State the blood parasite species.
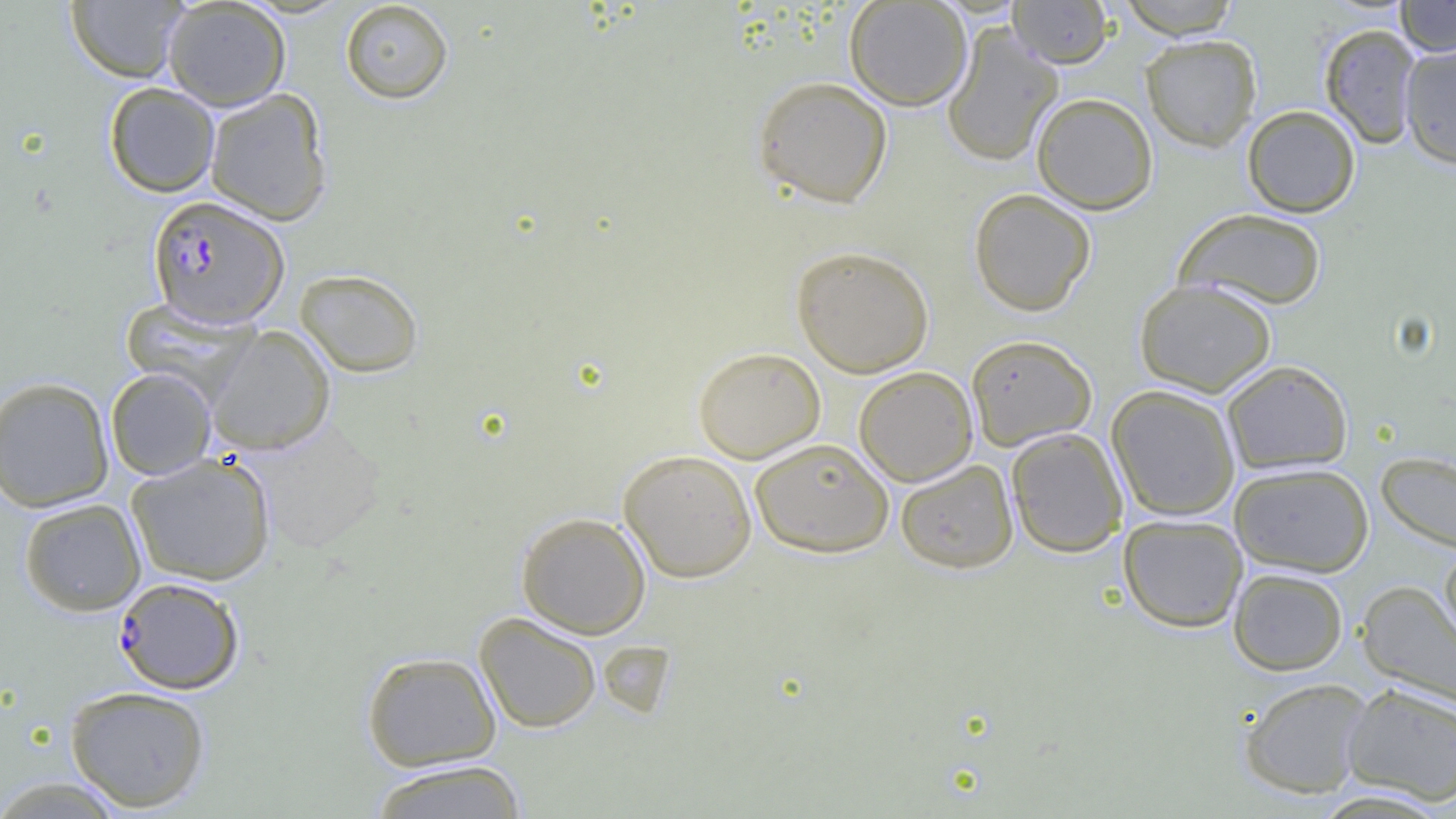
Plasmodium falciparum.

Summary:
  - Coordinate format: approximate bounding boxes as (x1,y1)-(x2,y2) corner pairs in pixels
  - Plasmodium falciparum-infected red blood cell locations: (148,195)-(289,328), (114,577)-(245,695)
  - Uninfected red blood cell locations: (65,0)-(189,83), (162,0)-(291,111), (844,0)-(972,111), (1008,0)-(1113,68), (1116,0)-(1242,38), (1395,0)-(1456,57), (339,1)-(454,104), (941,23)-(1063,167), (1318,23)-(1422,149), (1141,34)-(1262,152), (1399,42)-(1456,170), (753,76)-(893,208), (103,82)-(220,197), (204,88)-(332,226), (1031,92)-(1158,214), (1242,104)-(1360,217), (969,188)-(1096,316), (1174,208)-(1328,311), (791,245)-(934,377), (294,269)-(424,378), (1135,278)-(1277,396), (205,326)-(335,455), (965,334)-(1097,450), (693,346)-(826,463), (1221,360)-(1354,475), (854,366)-(978,486), (105,367)-(217,480), (0,376)-(115,512), (1106,384)-(1241,521), (247,419)-(388,554), (1006,427)-(1128,558), (750,437)-(894,557), (618,448)-(758,583), (1376,450)-(1456,555), (126,453)-(276,586), (895,458)-(1019,574), (1229,462)-(1374,577), (18,498)-(146,616), (516,511)-(651,639), (1118,514)-(1248,633), (1439,544)-(1456,654), (1228,567)-(1348,676), (1356,580)-(1456,708), (474,612)-(602,734), (361,651)-(502,771), (1238,677)-(1373,799), (1342,682)-(1456,805), (64,685)-(211,812), (365,759)-(530,819), (0,776)-(128,818)
  - Modality: optical microscopy
  - Magnification: 1000x
  - Image size: 1456×819 pixels
  - Field of view: one of a larger specimen
  - Preparation: thin blood smear